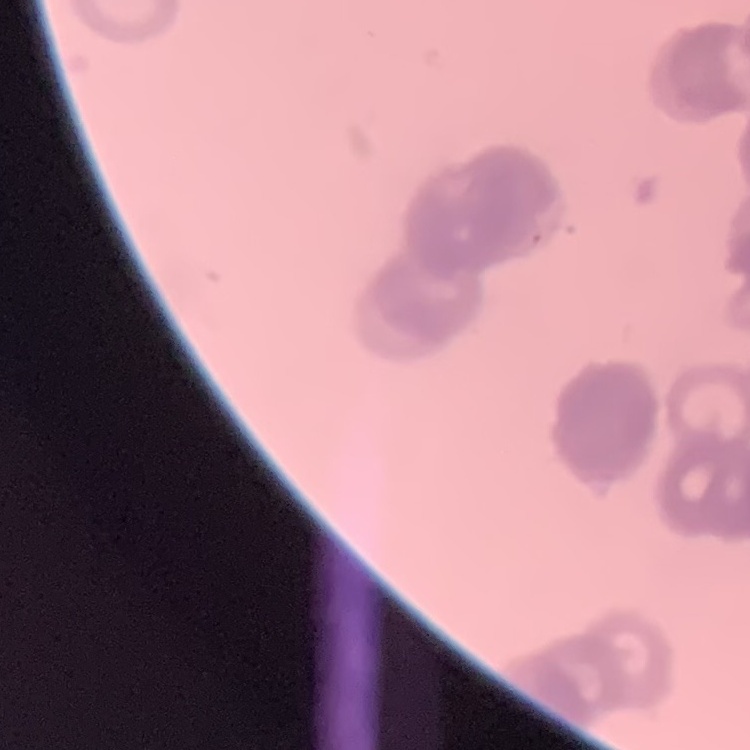

{
  "erythrocyte_morphology": "rouleaux formation",
  "image_type": "one tile cut from a larger photomicrograph",
  "preparation": "thin peripheral smear",
  "stain": "Field's or Giemsa"
}